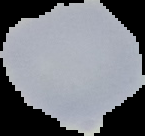
Summary:
  - Result: no malaria parasites detected
  - Preparation: thin blood film
  - Image type: segmented cell region with the area outside set to black
  - Image size: 145×136 pixels